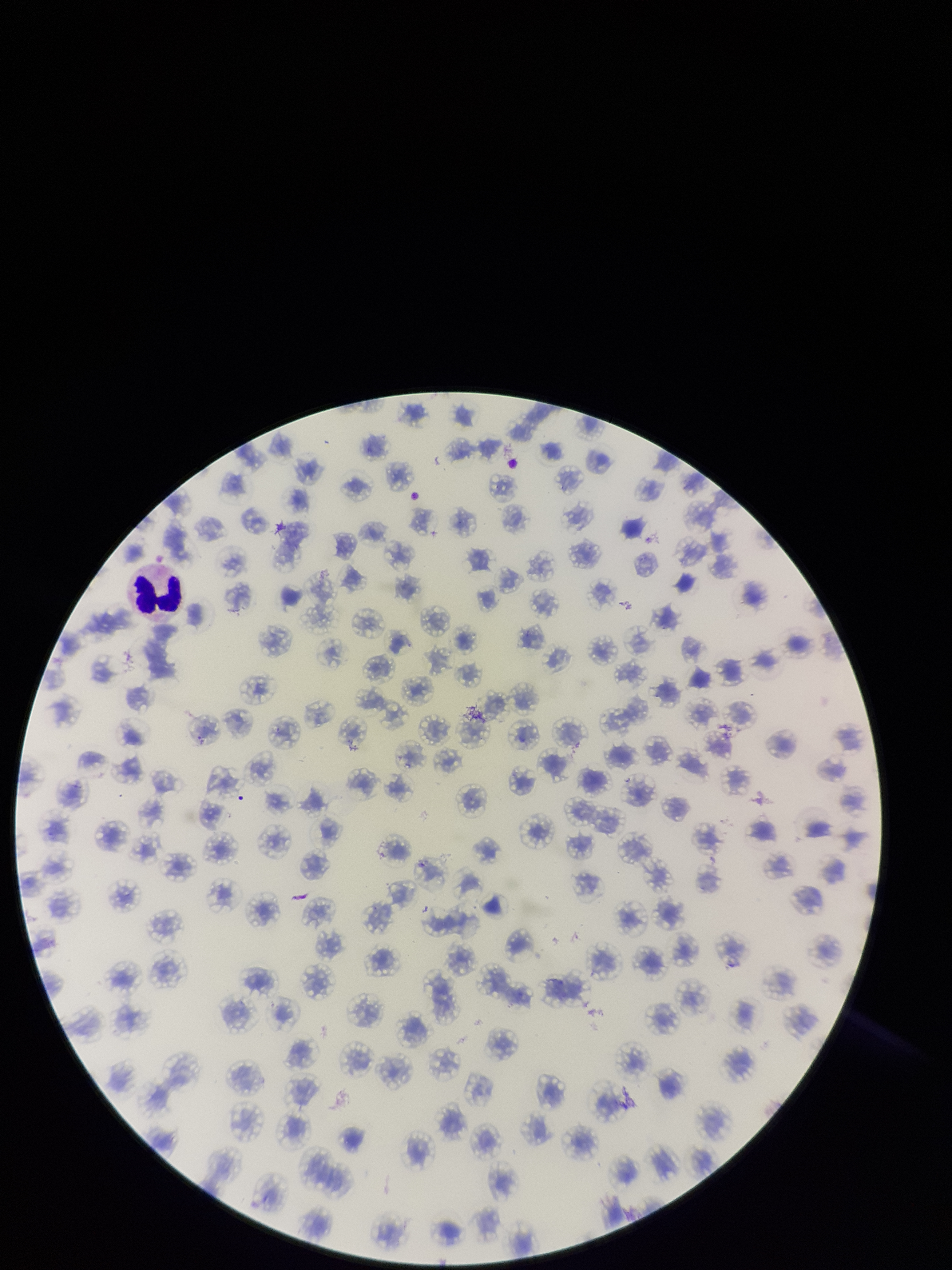
Summary:
  - Patient malaria status: infected
  - Red blood cell count: 150
  - Preparation: thin blood smear
  - Parasitized red blood cells: none identified
  - Field of view: one from this slide
  - Parasitized red blood cell count: 0
  - Image size: 952×1270 pixels
  - Stain: Giemsa
  - Capture: smartphone photograph through the microscope eyepiece
  - Species reported for this patient: Plasmodium falciparum